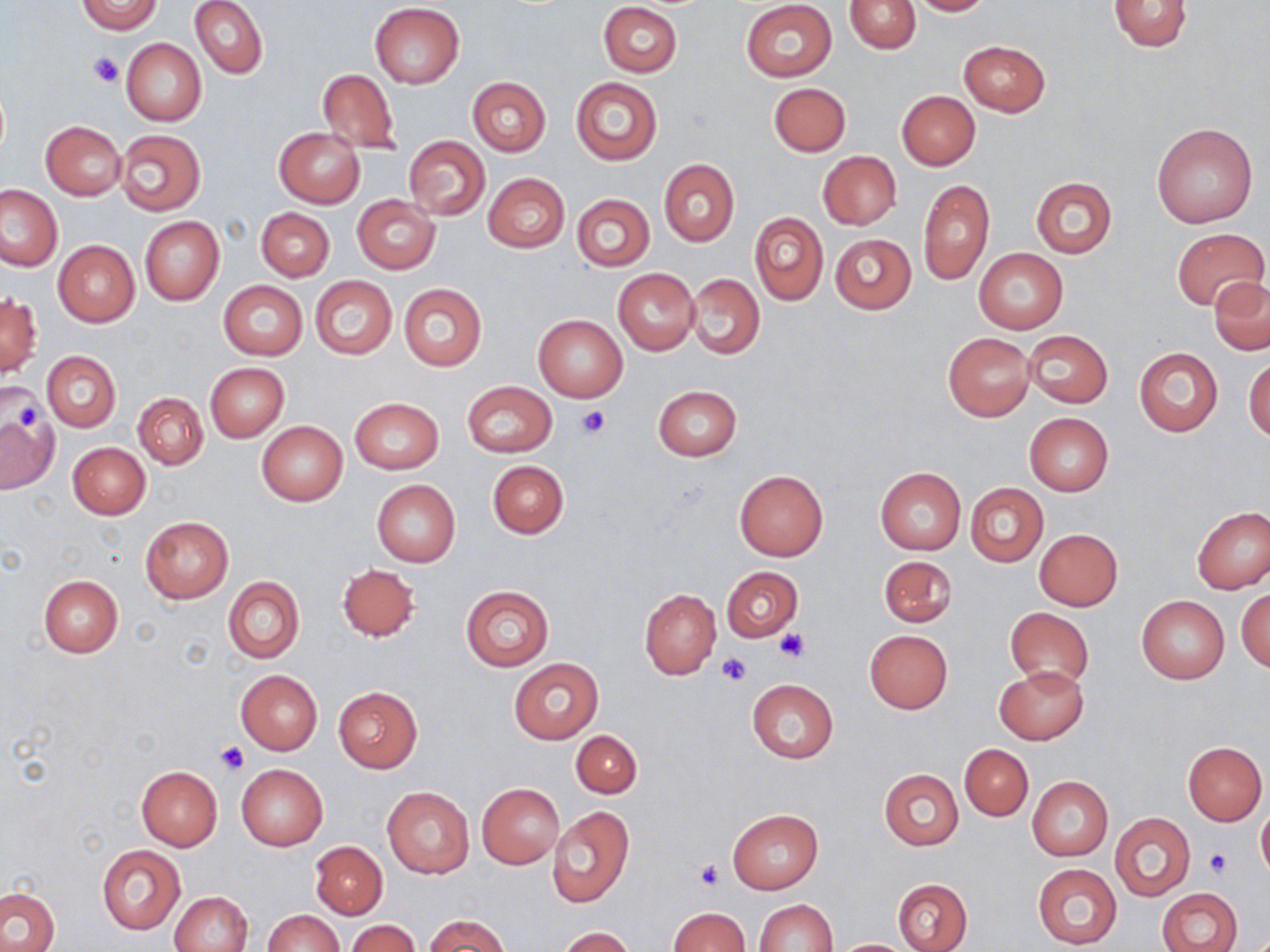
slide-level diagnosis = negative for blood parasites
image size = 1270×952 pixels
uninfected red blood cell locations = approximate bounding boxes as named x1/y1/x2/y2 corners in pixels: (x1=75, y1=0, x2=164, y2=34), (x1=190, y1=0, x2=267, y2=79), (x1=846, y1=0, x2=920, y2=54), (x1=905, y1=0, x2=994, y2=15), (x1=1108, y1=0, x2=1193, y2=51), (x1=598, y1=1, x2=682, y2=77), (x1=741, y1=1, x2=838, y2=82), (x1=370, y1=2, x2=464, y2=87), (x1=122, y1=39, x2=205, y2=125), (x1=959, y1=40, x2=1050, y2=116), (x1=317, y1=69, x2=399, y2=154), (x1=569, y1=77, x2=663, y2=166), (x1=467, y1=78, x2=550, y2=156), (x1=767, y1=82, x2=851, y2=156), (x1=897, y1=91, x2=980, y2=169), (x1=41, y1=121, x2=125, y2=198), (x1=1152, y1=122, x2=1257, y2=227), (x1=274, y1=127, x2=365, y2=208), (x1=116, y1=128, x2=205, y2=215), (x1=404, y1=136, x2=489, y2=220), (x1=819, y1=151, x2=901, y2=229), (x1=659, y1=159, x2=739, y2=246), (x1=483, y1=173, x2=569, y2=253), (x1=1030, y1=177, x2=1117, y2=258), (x1=917, y1=178, x2=994, y2=285), (x1=0, y1=184, x2=64, y2=271), (x1=571, y1=193, x2=654, y2=271), (x1=352, y1=195, x2=441, y2=274), (x1=256, y1=207, x2=334, y2=281), (x1=750, y1=213, x2=828, y2=305), (x1=139, y1=216, x2=224, y2=305), (x1=1171, y1=227, x2=1268, y2=310), (x1=829, y1=234, x2=915, y2=314), (x1=54, y1=241, x2=139, y2=326), (x1=973, y1=247, x2=1068, y2=334), (x1=612, y1=268, x2=699, y2=356), (x1=686, y1=274, x2=764, y2=359), (x1=310, y1=276, x2=396, y2=358), (x1=1209, y1=277, x2=1270, y2=354), (x1=218, y1=281, x2=308, y2=361), (x1=398, y1=282, x2=487, y2=372), (x1=1, y1=294, x2=41, y2=380), (x1=532, y1=313, x2=628, y2=402), (x1=1023, y1=330, x2=1112, y2=408), (x1=943, y1=332, x2=1035, y2=421), (x1=1133, y1=346, x2=1223, y2=437), (x1=42, y1=351, x2=121, y2=432), (x1=1245, y1=358, x2=1270, y2=443), (x1=205, y1=363, x2=289, y2=441), (x1=462, y1=381, x2=557, y2=458), (x1=653, y1=385, x2=742, y2=461), (x1=133, y1=392, x2=207, y2=469), (x1=349, y1=397, x2=444, y2=474), (x1=1, y1=413, x2=60, y2=493), (x1=1024, y1=413, x2=1113, y2=495), (x1=257, y1=421, x2=347, y2=505), (x1=67, y1=443, x2=150, y2=520), (x1=487, y1=460, x2=569, y2=538), (x1=876, y1=467, x2=965, y2=556), (x1=734, y1=469, x2=828, y2=561), (x1=371, y1=480, x2=460, y2=567), (x1=966, y1=483, x2=1047, y2=566), (x1=1192, y1=505, x2=1270, y2=594), (x1=140, y1=516, x2=232, y2=603), (x1=1035, y1=528, x2=1123, y2=610), (x1=879, y1=555, x2=957, y2=628), (x1=336, y1=565, x2=420, y2=642), (x1=722, y1=567, x2=803, y2=639), (x1=39, y1=574, x2=123, y2=658), (x1=223, y1=576, x2=305, y2=664), (x1=460, y1=585, x2=554, y2=672), (x1=1237, y1=589, x2=1270, y2=672), (x1=639, y1=590, x2=720, y2=678), (x1=1136, y1=596, x2=1230, y2=683), (x1=1006, y1=608, x2=1093, y2=686), (x1=864, y1=629, x2=953, y2=713), (x1=509, y1=658, x2=603, y2=743), (x1=995, y1=666, x2=1089, y2=744), (x1=235, y1=670, x2=323, y2=755), (x1=746, y1=679, x2=839, y2=763), (x1=333, y1=688, x2=422, y2=771), (x1=572, y1=730, x2=642, y2=798), (x1=1183, y1=741, x2=1267, y2=825), (x1=959, y1=744, x2=1033, y2=821), (x1=136, y1=764, x2=222, y2=850), (x1=237, y1=764, x2=327, y2=850), (x1=880, y1=769, x2=963, y2=849), (x1=1026, y1=776, x2=1113, y2=861), (x1=477, y1=783, x2=563, y2=867), (x1=382, y1=786, x2=475, y2=879), (x1=1256, y1=802, x2=1270, y2=883), (x1=547, y1=805, x2=634, y2=907), (x1=727, y1=809, x2=822, y2=894), (x1=1110, y1=812, x2=1195, y2=901), (x1=309, y1=840, x2=388, y2=919), (x1=97, y1=845, x2=185, y2=933), (x1=1034, y1=864, x2=1121, y2=948), (x1=894, y1=878, x2=972, y2=952), (x1=1, y1=888, x2=59, y2=952), (x1=1157, y1=888, x2=1242, y2=952), (x1=170, y1=891, x2=253, y2=952), (x1=754, y1=898, x2=837, y2=951), (x1=667, y1=906, x2=750, y2=951), (x1=263, y1=909, x2=344, y2=952), (x1=423, y1=914, x2=512, y2=952), (x1=345, y1=919, x2=421, y2=952), (x1=557, y1=927, x2=636, y2=952), (x1=828, y1=939, x2=918, y2=951)
modality = optical microscopy
stain = May-Grünwald-Giemsa
field of view = single
platelet locations = approximate bounding boxes as named x1/y1/x2/y2 corners in pixels: (x1=89, y1=52, x2=124, y2=88), (x1=6, y1=388, x2=48, y2=439), (x1=575, y1=407, x2=610, y2=439), (x1=773, y1=627, x2=811, y2=664), (x1=716, y1=651, x2=751, y2=687), (x1=216, y1=741, x2=249, y2=774), (x1=1205, y1=849, x2=1232, y2=877), (x1=695, y1=859, x2=725, y2=890)
magnification = 1000x
preparation = thin blood film